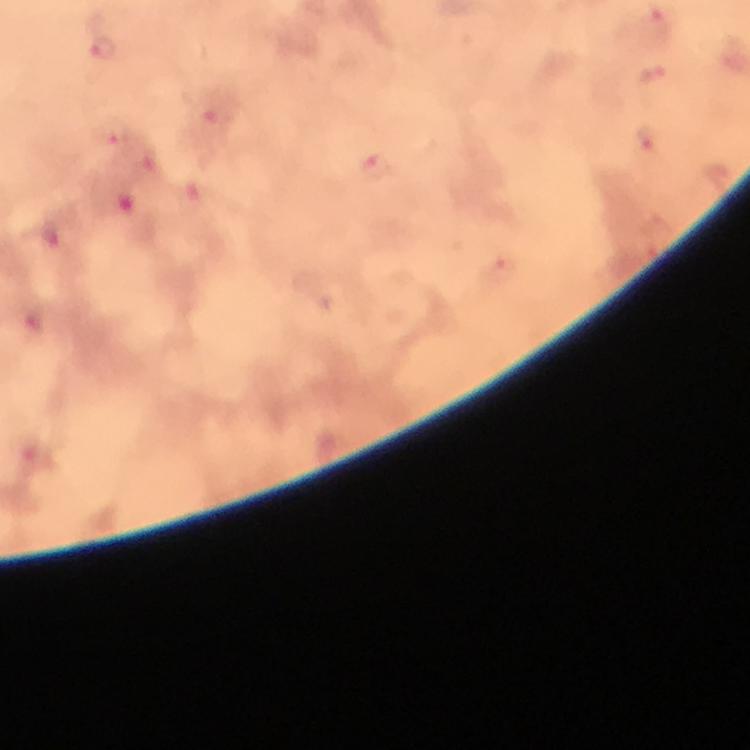

Approximate centers as [x, y] in pixels. Plasmodium parasite locations: [656, 25], [105, 47], [652, 77], [111, 134], [646, 142], [374, 168], [53, 242], [502, 273], [35, 325]. At 100x magnification. From a malaria diagnostic workup. Cropped region of a single field of view. Thick blood smear. Giemsa-stained preparation. Image is 750×750 pixels. Immersion oil was used. Photographed with a smartphone mounted on the microscope.